Name the cell type shown.
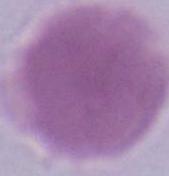

This is an erythrocyte.

Photomicrograph. 1000x magnification.